State which parasite is depicted.
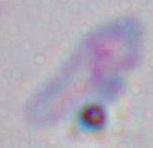
Toxoplasma gondii.

Captured at 1000x magnification. Photomicrograph.